Identify the parasite.
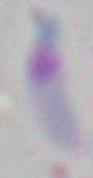
Toxoplasma gondii.

modality = micrograph
magnification = 1000x